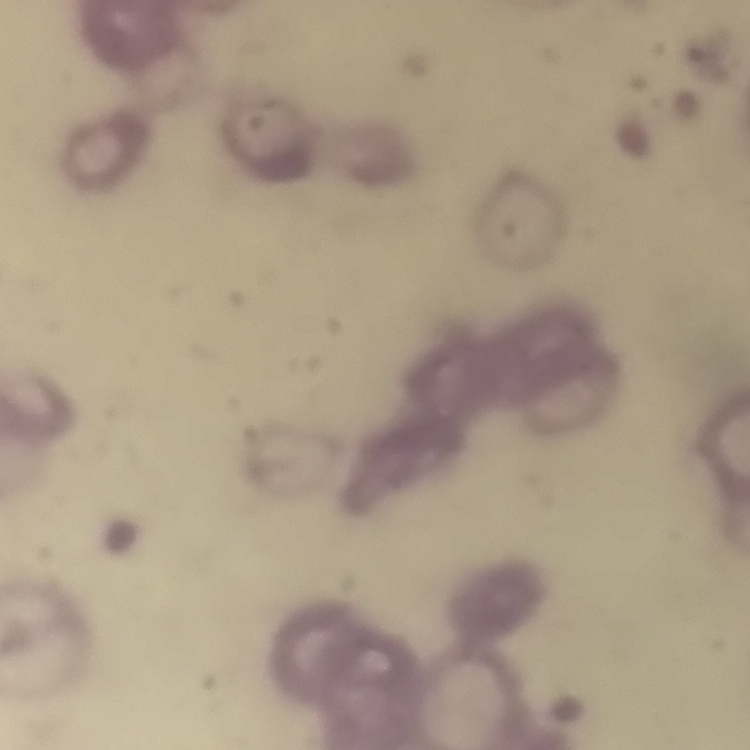
Summary:
  - Erythrocyte morphology: rouleaux formation
  - Image type: square crop of a larger photomicrograph
  - Preparation: thin peripheral smear
  - Stain: Field's or Giemsa